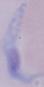
1000x magnification. Photomicrograph. A trypanosome is shown.